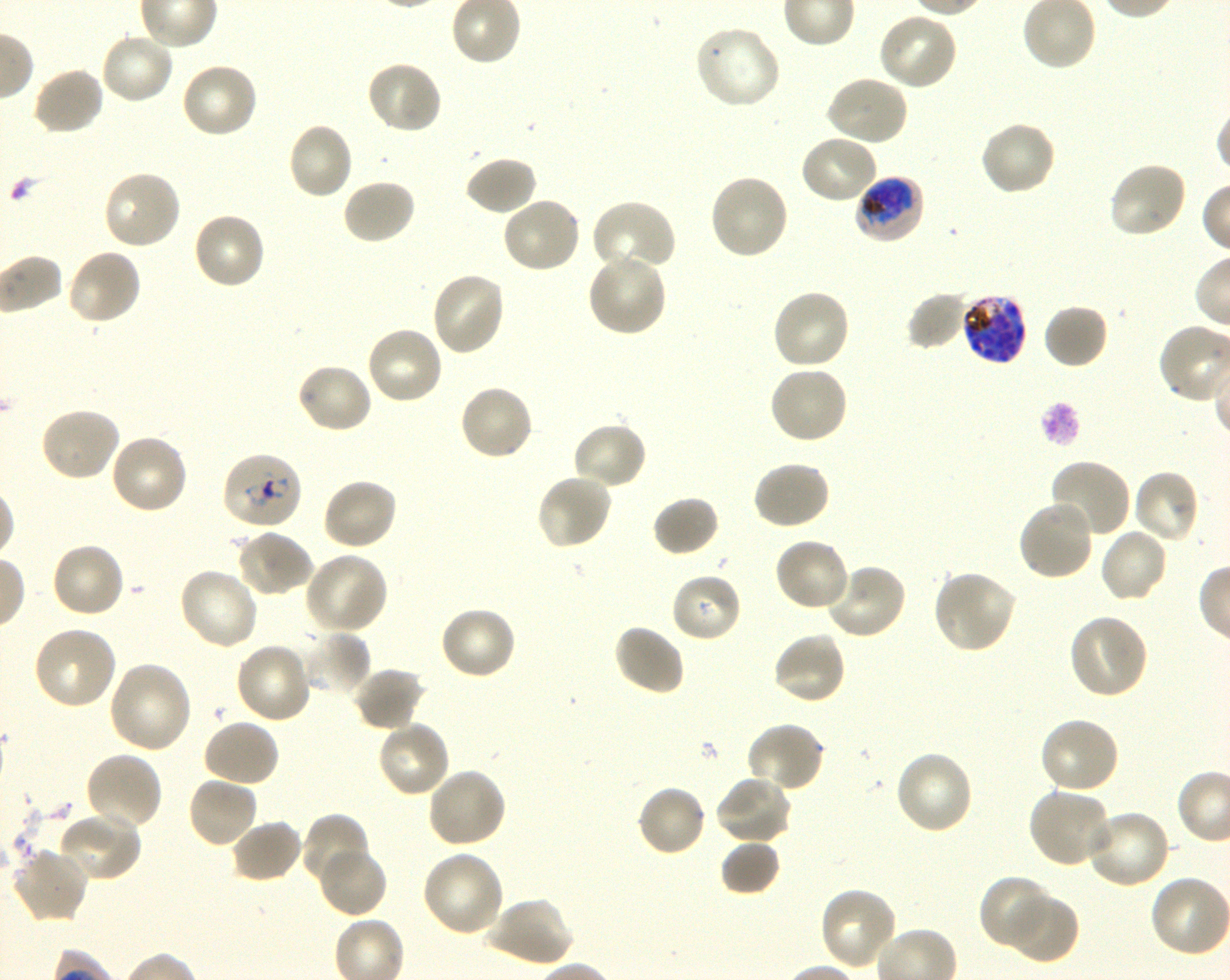

Approximate bounding boxes as [x1, y1, x2, y2] in pixels. Not every red blood cell is marked. A life-cycle stage — or a range of stages, where the recorded stages span more than one — follows each staged infected red blood cell.
Summary:
  - Locations of infected red blood cells: [854, 174, 925, 245] early trophozoite to early schizont; [960, 291, 1028, 365] schizont; [221, 452, 303, 531] ring
  - Locations of uninfected red blood cells: [876, 12, 958, 92], [694, 24, 782, 111], [99, 30, 176, 106], [365, 60, 444, 135], [180, 62, 260, 139], [32, 68, 105, 137], [824, 75, 909, 147], [978, 120, 1057, 197], [286, 121, 354, 201], [798, 133, 879, 206], [463, 155, 538, 216], [1108, 161, 1188, 240], [102, 170, 183, 251], [708, 173, 789, 261], [341, 177, 417, 246], [501, 196, 583, 275], [589, 199, 677, 275], [192, 211, 268, 291], [65, 248, 142, 326], [586, 252, 667, 337], [430, 270, 506, 357], [771, 287, 851, 370], [907, 292, 969, 351], [1042, 304, 1109, 371], [365, 326, 444, 406], [295, 362, 374, 434], [767, 365, 849, 445], [458, 384, 534, 461], [38, 406, 122, 482], [571, 421, 648, 491], [109, 433, 189, 515], [1049, 458, 1131, 539], [751, 459, 830, 531], [1132, 469, 1201, 544], [535, 473, 613, 551], [321, 477, 398, 552], [652, 494, 721, 557], [1016, 498, 1095, 582], [1099, 526, 1169, 604], [234, 528, 314, 598], [773, 536, 850, 612], [49, 542, 125, 620], [304, 552, 388, 635], [823, 563, 907, 640], [177, 567, 260, 651], [931, 568, 1017, 654], [670, 572, 742, 644], [438, 605, 518, 680], [1067, 613, 1150, 700], [612, 623, 686, 696], [31, 625, 117, 711], [303, 630, 371, 699], [772, 632, 847, 706], [233, 642, 313, 725], [108, 660, 193, 754], [352, 667, 426, 731], [1038, 717, 1121, 795], [202, 718, 280, 789], [376, 719, 451, 799], [745, 722, 825, 794], [894, 749, 975, 835], [84, 751, 163, 831], [426, 767, 508, 849], [715, 774, 793, 845], [186, 775, 259, 849], [636, 783, 708, 858], [1028, 787, 1116, 868], [1084, 808, 1171, 889], [300, 811, 371, 889], [58, 812, 142, 884], [230, 819, 304, 884], [720, 839, 780, 896], [317, 846, 388, 919], [11, 847, 88, 925], [421, 850, 505, 939], [980, 874, 1053, 950], [819, 886, 900, 971], [1003, 893, 1079, 964], [484, 896, 573, 968]
  - Life-cycle stages observed: ring, schizont
  - Stain: Giemsa
  - Objective: 100x, oil immersion, numerical aperture 1.30
  - Preparation: thin blood smear
  - Donor blood group: O+
  - Culture: shaking in-vitro Plasmodium falciparum strain 3D7
  - Image size: 1230×980 pixels
  - Field of view: one from this slide